Give the extent of all Trypanosoma brucei.
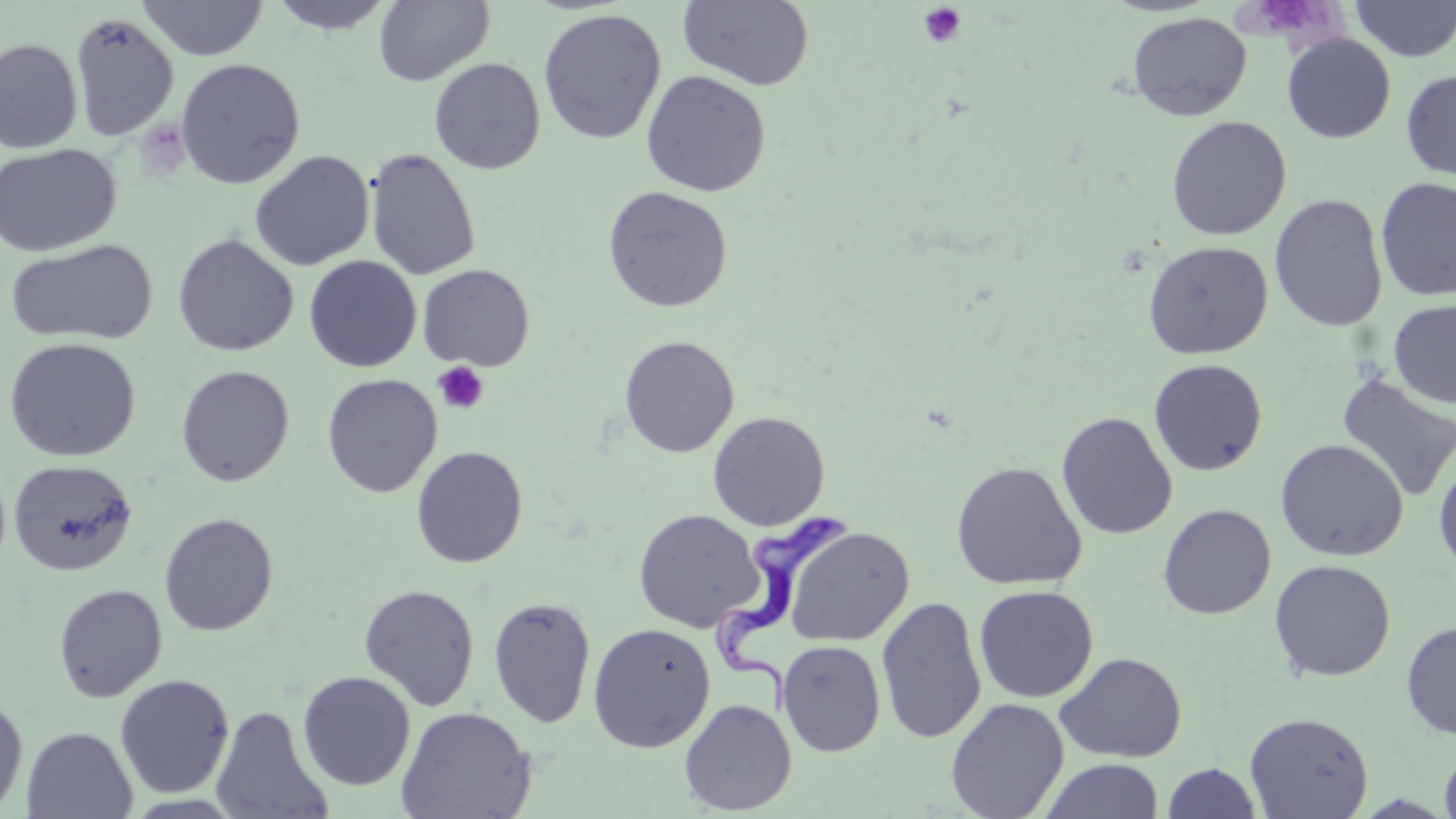
Approximate bounding boxes as [x1, y1, x2, y2] in pixels.
Trypanosoma brucei: [713, 502, 857, 725].

Summary:
  - Uninfected red blood cell locations: [266, 0, 396, 35], [677, 0, 815, 91], [1350, 0, 1456, 62], [138, 1, 268, 61], [373, 1, 494, 86], [537, 8, 667, 145], [69, 11, 179, 142], [1127, 12, 1252, 122], [1282, 33, 1396, 144], [0, 38, 83, 153], [428, 57, 546, 175], [174, 58, 306, 189], [1400, 68, 1456, 183], [640, 70, 771, 197], [1166, 115, 1292, 240], [0, 143, 121, 257], [364, 147, 481, 281], [249, 150, 374, 271], [1376, 176, 1456, 302], [602, 185, 734, 313], [1270, 193, 1388, 332], [172, 233, 299, 357], [5, 239, 158, 346], [1142, 240, 1274, 360], [304, 255, 422, 373], [417, 264, 535, 371], [1388, 299, 1456, 409], [619, 335, 739, 458], [3, 337, 141, 462], [1148, 358, 1268, 476], [175, 365, 295, 486], [1335, 371, 1456, 503], [321, 373, 442, 498], [707, 411, 831, 530], [1056, 411, 1178, 541], [1275, 438, 1409, 562], [411, 445, 528, 568], [1433, 452, 1456, 577], [7, 459, 138, 576], [950, 460, 1087, 590], [1157, 503, 1277, 620], [633, 509, 764, 633], [158, 513, 278, 636], [783, 526, 913, 647], [1269, 559, 1396, 682], [52, 583, 168, 703], [358, 584, 480, 711], [974, 584, 1098, 703], [487, 596, 597, 729], [876, 596, 987, 744], [1401, 618, 1456, 741], [588, 622, 716, 753], [777, 640, 886, 757], [1055, 651, 1187, 763], [297, 670, 416, 790], [114, 674, 235, 798], [0, 693, 28, 815], [945, 697, 1070, 819], [679, 698, 796, 815], [211, 704, 335, 819], [396, 706, 536, 818], [1244, 711, 1374, 819], [21, 726, 138, 818], [1439, 743, 1456, 819], [1038, 758, 1165, 819], [1162, 761, 1262, 819]
  - Platelet locations: [918, 3, 967, 48], [432, 362, 489, 415]
  - Slide-level diagnosis: Trypanosoma brucei
  - Stain: May-Grünwald-Giemsa
  - Preparation: thin blood film
  - Modality: optical microscopy
  - Image size: 1456×819 pixels
  - Magnification: 1000x
  - Field of view: single